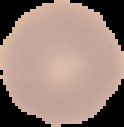

Summary:
  - Image size: 124×127 pixels
  - Result: no malaria parasites seen
  - Preparation: thin blood film
  - Image type: segmented cell region with the area outside set to black